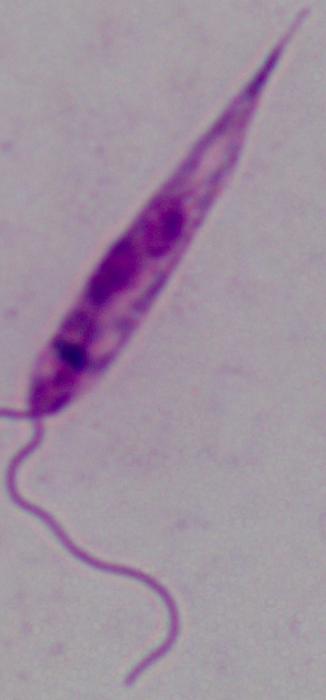

{
  "identification": "Leishmania",
  "modality": "photomicrograph",
  "magnification": "1000x"
}